Comment on the morphology of the red blood cells.
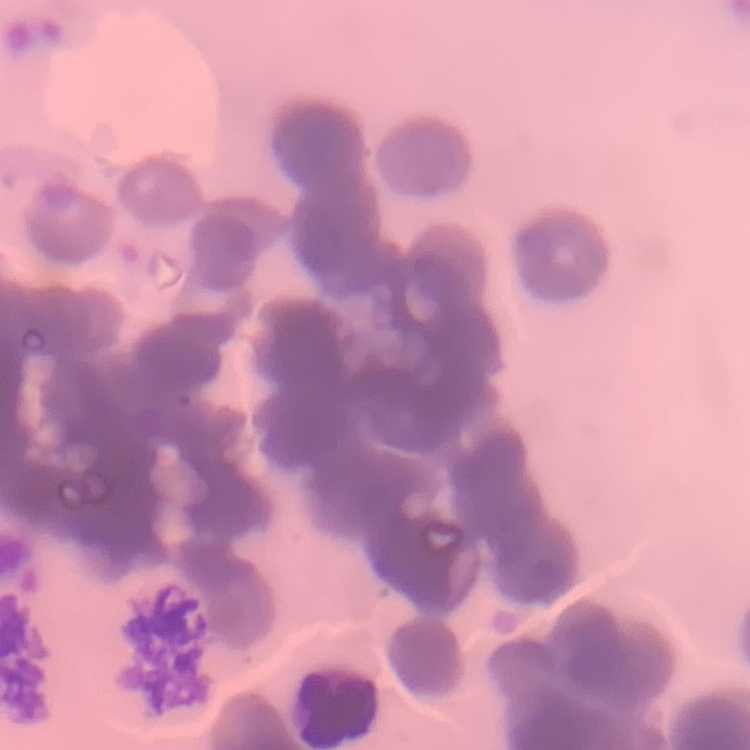

Rouleaux formation.

preparation = thin blood smear
stain = Field's or Giemsa
image type = square crop of a larger photomicrograph